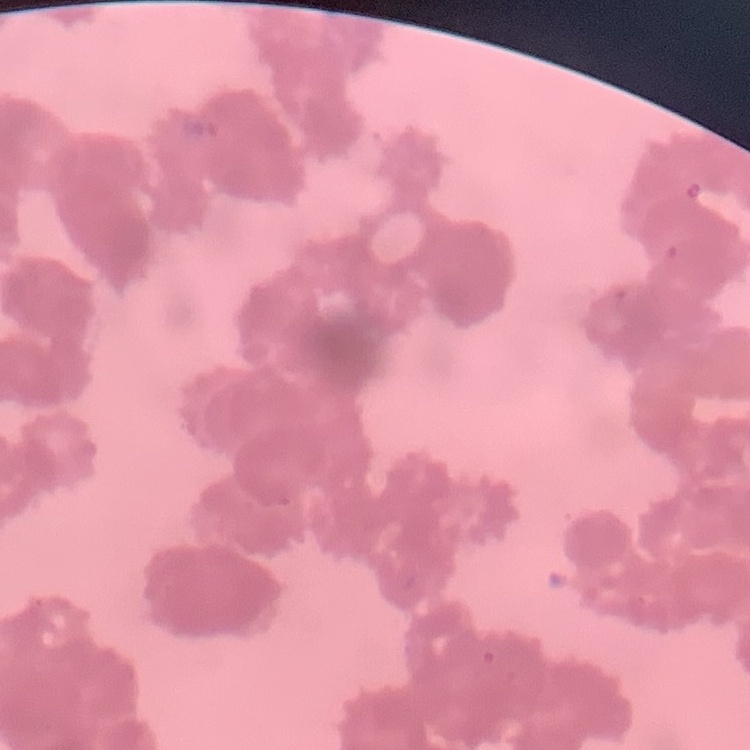
red_blood_cell_morphology: rouleaux formation
preparation: thin blood film
image_type: square crop of a larger photomicrograph
stain: Field's or Giemsa